Report the malaria status of this cell.
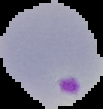

Parasitized.

From a thin blood film. Segmented cell region on a black background. Image is 103×109 pixels.